Assess this cell for malaria.
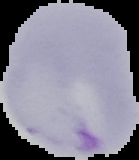
Parasitized.

image_size: 139×160 pixels
image_type: segmented cell region with the area outside set to black
preparation: thin blood smear